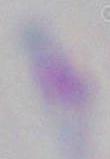

magnification = 1000x
modality = micrograph
identification = Toxoplasma gondii